Outline each Plasmodium vivax-infected red blood cell.
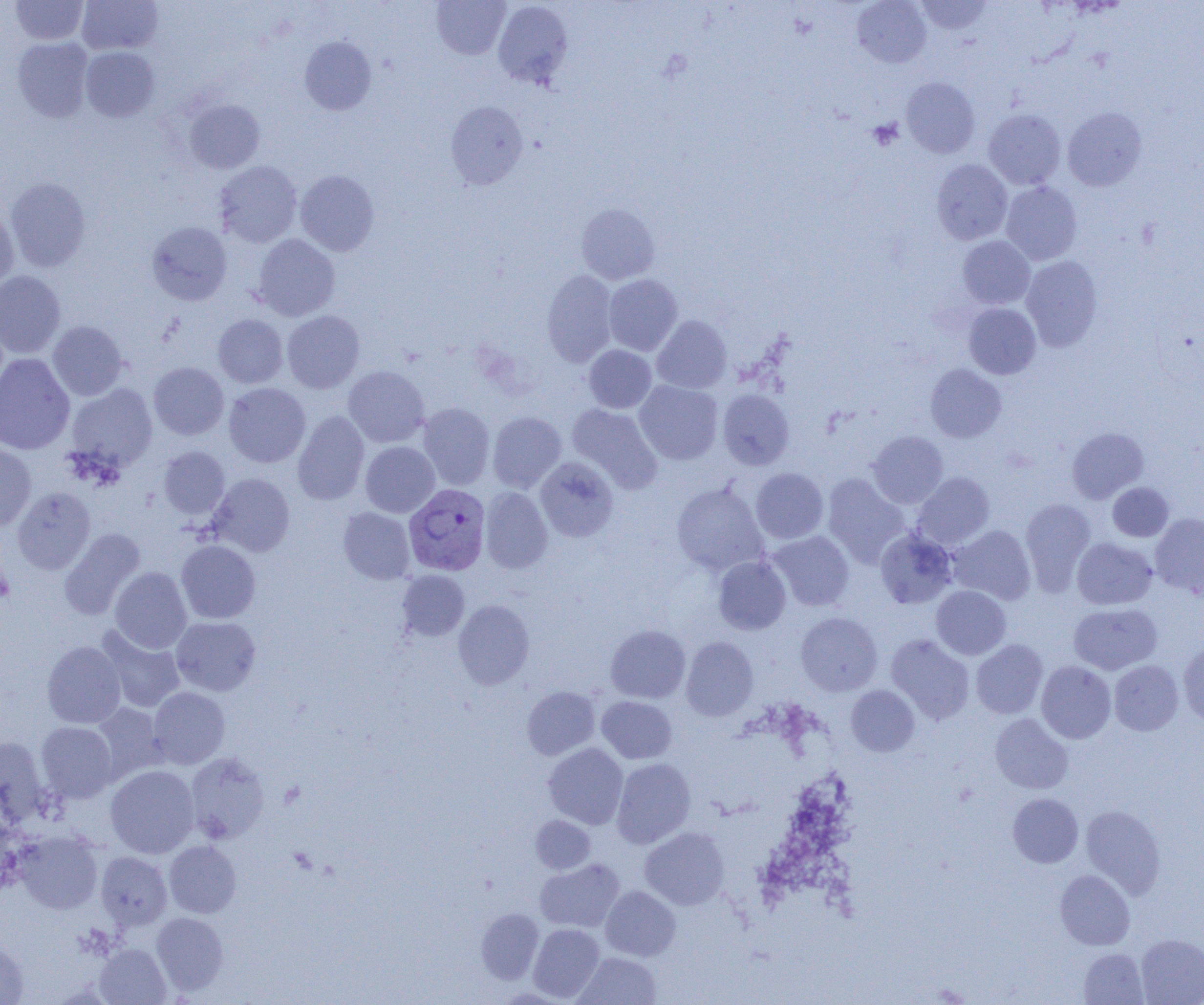

Approximate bounding boxes as (x1, y1, x2, y2) in pixels.
Plasmodium vivax-infected red blood cells: (404, 483, 491, 575).

slide-level diagnosis = Plasmodium vivax
uninfected red blood cell locations = approximate bounding boxes as (x1, y1, x2, y2) in pixels: (10, 0, 89, 45), (431, 0, 511, 60), (852, 0, 931, 68), (916, 0, 992, 34), (77, 1, 163, 55), (493, 1, 573, 88), (299, 36, 377, 116), (12, 37, 94, 122), (80, 47, 159, 122), (901, 77, 979, 158), (183, 99, 265, 173), (446, 101, 528, 189), (1063, 107, 1147, 191), (983, 109, 1066, 190), (931, 159, 1012, 244), (215, 161, 302, 247), (294, 170, 379, 256), (5, 178, 91, 272), (1001, 182, 1082, 265), (576, 203, 659, 284), (0, 207, 18, 294), (146, 221, 232, 305), (252, 234, 340, 321), (958, 236, 1035, 309), (1021, 255, 1103, 352), (542, 269, 618, 367), (0, 270, 65, 358), (603, 274, 682, 355), (963, 303, 1041, 379), (281, 310, 364, 393), (213, 314, 288, 388), (652, 315, 732, 393), (48, 320, 128, 401), (583, 345, 656, 413), (0, 353, 75, 455), (149, 362, 229, 440), (926, 364, 1006, 442), (343, 366, 430, 447), (635, 380, 722, 465), (224, 383, 310, 467), (67, 384, 157, 471), (717, 389, 794, 470), (417, 403, 495, 490), (567, 404, 662, 493), (292, 411, 369, 505), (487, 411, 566, 493), (1067, 426, 1149, 504), (868, 430, 948, 508), (360, 441, 440, 517), (0, 444, 36, 530), (158, 446, 230, 519), (535, 457, 618, 542), (750, 468, 828, 544), (913, 472, 995, 549), (208, 473, 295, 557), (822, 474, 909, 567), (671, 481, 769, 576), (1108, 482, 1174, 541), (12, 487, 95, 574), (480, 487, 552, 573), (1020, 498, 1096, 594), (338, 507, 415, 584), (1150, 513, 1204, 598), (949, 525, 1036, 604), (59, 528, 145, 620), (875, 528, 958, 609), (767, 531, 855, 611), (1072, 537, 1157, 609), (176, 540, 261, 623), (713, 556, 791, 635), (110, 567, 192, 653), (397, 570, 470, 641), (931, 585, 1011, 659), (454, 600, 534, 689), (1068, 603, 1162, 674), (796, 612, 882, 696), (171, 617, 260, 696), (605, 625, 690, 703), (97, 627, 185, 713), (886, 634, 975, 724), (681, 636, 758, 721), (971, 639, 1048, 718), (42, 641, 126, 728), (1178, 643, 1204, 727), (1109, 660, 1183, 735), (1036, 661, 1116, 743), (846, 685, 920, 756), (522, 686, 600, 759), (148, 687, 230, 769), (597, 696, 677, 763), (91, 703, 167, 782), (990, 713, 1073, 794), (36, 721, 117, 803), (0, 736, 50, 823), (544, 743, 628, 829), (185, 752, 269, 844), (612, 758, 695, 848), (105, 765, 199, 858), (1008, 793, 1083, 868), (1080, 804, 1166, 898), (530, 815, 595, 874), (640, 827, 729, 910), (13, 831, 103, 913), (164, 840, 241, 917), (96, 852, 172, 930), (535, 858, 625, 933), (1055, 870, 1135, 950), (601, 886, 681, 961), (476, 908, 544, 984), (151, 912, 228, 995), (528, 924, 605, 1001), (1136, 934, 1204, 1005), (0, 941, 29, 1004), (95, 944, 170, 1004), (1078, 948, 1148, 1004), (574, 952, 661, 1005)
field of view = one of a larger specimen
magnification = 1000x
preparation = thin blood film
image size = 1204×1005 pixels
platelet locations = approximate bounding boxes as (x1, y1, x2, y2) in pixels: (867, 119, 903, 150), (0, 562, 13, 606)
modality = optical microscopy